Describe the morphology of the red blood cells.
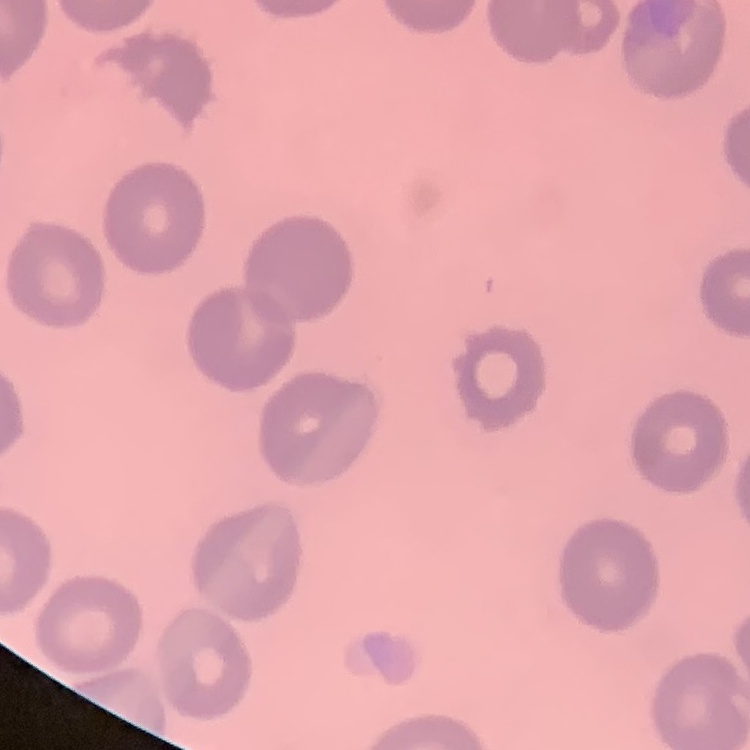
No rouleaux formation.

Summary:
  - Stain: Field's or Giemsa
  - Image type: square crop of a larger photomicrograph
  - Preparation: thin blood smear